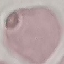
{
  "malaria_status": "uninfected",
  "image_type": "automatically extracted cell patch, resized to 64 × 64 pixels",
  "preparation": "thin smear",
  "stain": "Giemsa",
  "capture": "smartphone through the microscope eyepiece"
}